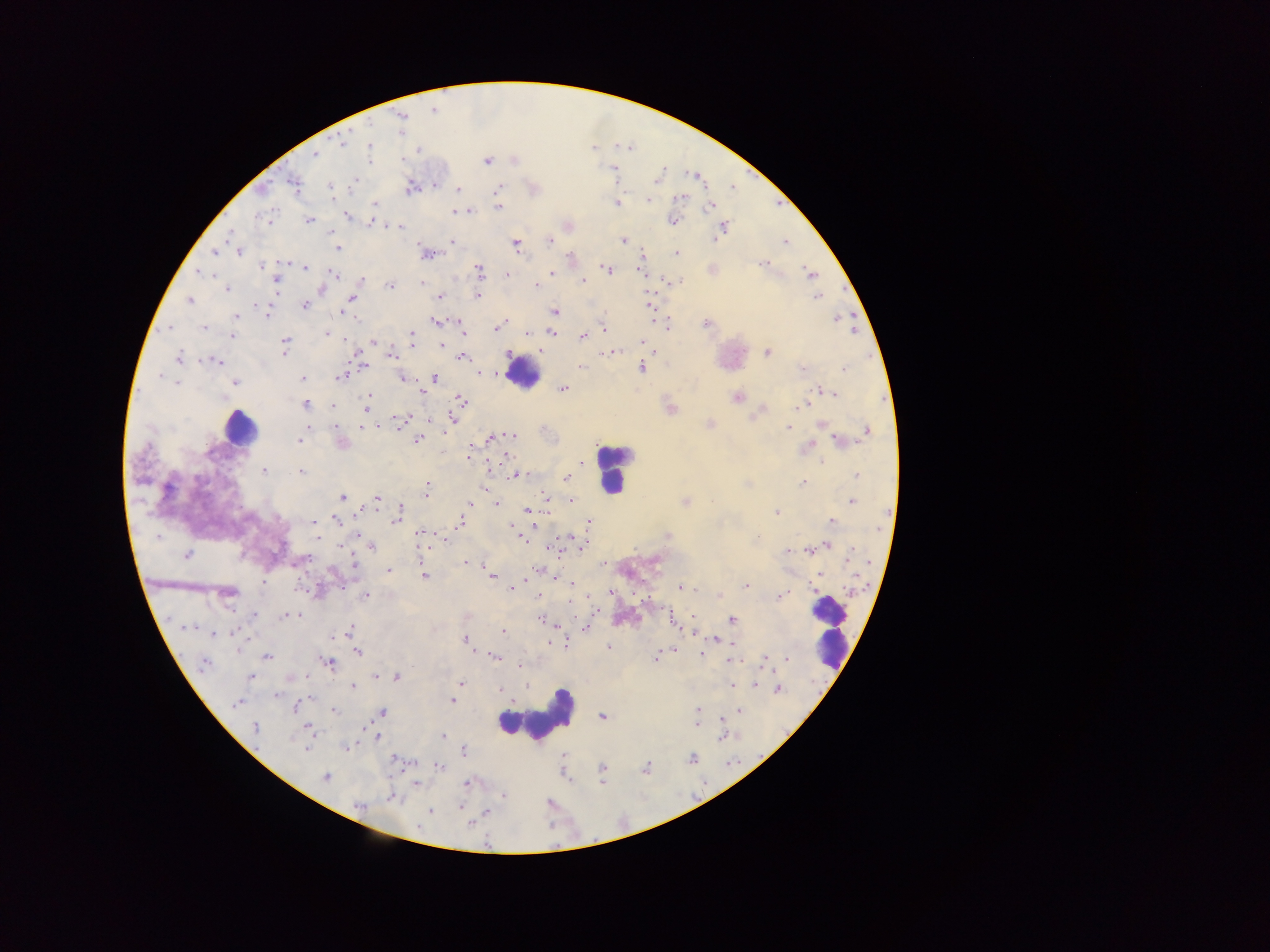

Approximate centers as {x, y} in pixels.
Summary:
  - Leukocyte locations: {522, 372}, {240, 427}, {613, 469}, {830, 627}, {536, 717}
  - Malaria parasite locations: {432, 110}, {400, 116}, {343, 142}, {369, 147}, {314, 156}, {367, 159}, {487, 161}, {614, 171}, {658, 178}, {293, 183}, {434, 185}, {330, 187}, {410, 187}, {458, 189}, {497, 192}, {680, 197}, {647, 200}, {615, 202}, {375, 205}, {711, 205}, {498, 207}, {456, 211}, {346, 215}, {308, 220}, {672, 220}, {371, 221}, {567, 225}, {399, 226}, {724, 226}, {623, 240}, {550, 241}, {451, 242}, {785, 242}, {515, 243}, {337, 247}, {238, 251}, {215, 252}, {676, 253}, {426, 254}, {571, 256}, {642, 257}, {764, 262}, {261, 266}, {305, 267}, {607, 269}, {479, 271}, {551, 272}, {199, 273}, {644, 273}, {811, 273}, {333, 274}, {505, 274}, {275, 280}, {361, 281}, {582, 281}, {422, 282}, {390, 285}, {534, 285}, {321, 288}, {226, 289}, {477, 295}, {816, 296}, {440, 297}, {351, 299}, {189, 300}, {304, 305}, {648, 305}, {266, 309}, {554, 312}, {343, 313}, {236, 315}, {836, 319}, {436, 321}, {706, 324}, {496, 326}, {666, 326}, {203, 327}, {171, 328}, {604, 329}, {460, 330}, {550, 332}, {327, 333}, {527, 333}, {232, 336}, {583, 336}, {411, 337}, {285, 342}, {374, 342}, {640, 342}, {441, 345}, {540, 350}, {602, 351}, {615, 352}, {653, 352}, {767, 352}, {391, 354}, {462, 356}, {177, 359}, {215, 360}, {362, 366}, {580, 367}, {640, 367}, {802, 368}, {845, 368}, {479, 374}, {302, 377}, {342, 377}, {402, 377}, {435, 378}, {177, 383}, {235, 383}, {563, 389}, {823, 391}, {369, 392}, {422, 393}, {833, 393}, {367, 397}, {736, 397}, {461, 400}, {304, 404}, {804, 405}, {330, 407}, {366, 407}, {670, 408}, {762, 409}, {393, 418}, {404, 418}, {452, 419}, {397, 420}, {822, 423}, {709, 424}, {335, 425}, {363, 425}, {788, 426}, {866, 430}, {510, 434}, {417, 438}, {490, 438}, {298, 440}, {839, 441}, {341, 442}, {808, 446}, {469, 454}, {505, 456}, {821, 461}, {582, 464}, {264, 471}, {300, 471}, {514, 475}, {857, 475}, {565, 478}, {802, 481}, {748, 484}, {427, 486}, {482, 488}, {425, 492}, {342, 496}, {377, 497}, {547, 498}, {571, 501}, {685, 501}, {851, 501}, {495, 503}, {470, 504}, {398, 510}, {527, 510}, {776, 512}, {830, 520}, {313, 522}, {336, 522}, {589, 522}, {459, 524}, {536, 527}, {515, 533}, {419, 534}, {357, 535}, {667, 536}, {316, 537}, {520, 537}, {756, 537}, {571, 538}, {445, 539}, {827, 544}, {583, 545}, {372, 547}, {582, 549}, {787, 550}, {807, 550}, {555, 551}, {187, 554}, {299, 561}, {465, 562}, {353, 564}, {537, 569}, {388, 570}, {491, 575}, {553, 575}, {820, 575}, {424, 576}, {571, 583}, {745, 585}, {679, 587}, {510, 588}, {226, 592}, {610, 592}, {366, 595}, {781, 595}, {537, 597}, {718, 597}, {254, 615}, {286, 615}, {692, 615}, {670, 619}, {732, 619}, {542, 620}, {555, 624}, {693, 629}, {585, 630}, {348, 632}, {503, 632}, {212, 633}, {465, 639}, {715, 639}, {735, 645}, {607, 647}, {674, 649}, {358, 651}, {701, 654}, {493, 655}, {267, 656}, {764, 656}, {655, 658}, {787, 659}, {730, 661}, {203, 663}, {328, 663}, {519, 666}, {377, 675}, {396, 676}, {250, 677}, {461, 684}, {756, 684}, {731, 685}, {352, 687}, {777, 688}, {499, 689}, {275, 695}, {452, 701}, {237, 703}, {296, 706}, {698, 709}, {333, 710}, {739, 710}, {382, 712}, {601, 716}, {721, 717}, {695, 725}, {255, 728}, {308, 729}, {443, 735}, {723, 735}, {377, 736}, {346, 746}, {305, 747}, {464, 749}, {692, 758}, {394, 759}, {439, 766}, {602, 767}, {646, 767}, {326, 777}, {601, 781}, {416, 783}, {467, 783}, {503, 796}, {392, 797}, {460, 805}, {359, 806}, {431, 811}, {487, 813}, {470, 823}
  - Country: Ghana
  - Capture: mobile-phone photograph through a microscope
  - Image size: 1270×952 pixels
  - Preparation: thick blood smear
  - Field of view: single